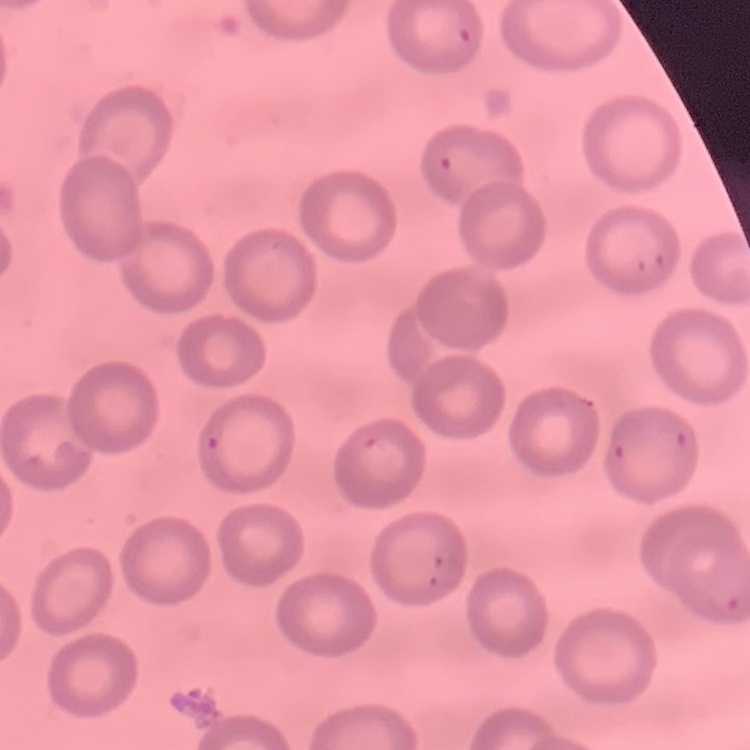

red blood cell morphology = no rouleaux formation
image type = square crop of a larger photomicrograph
preparation = thin blood film
stain = Field's or Giemsa